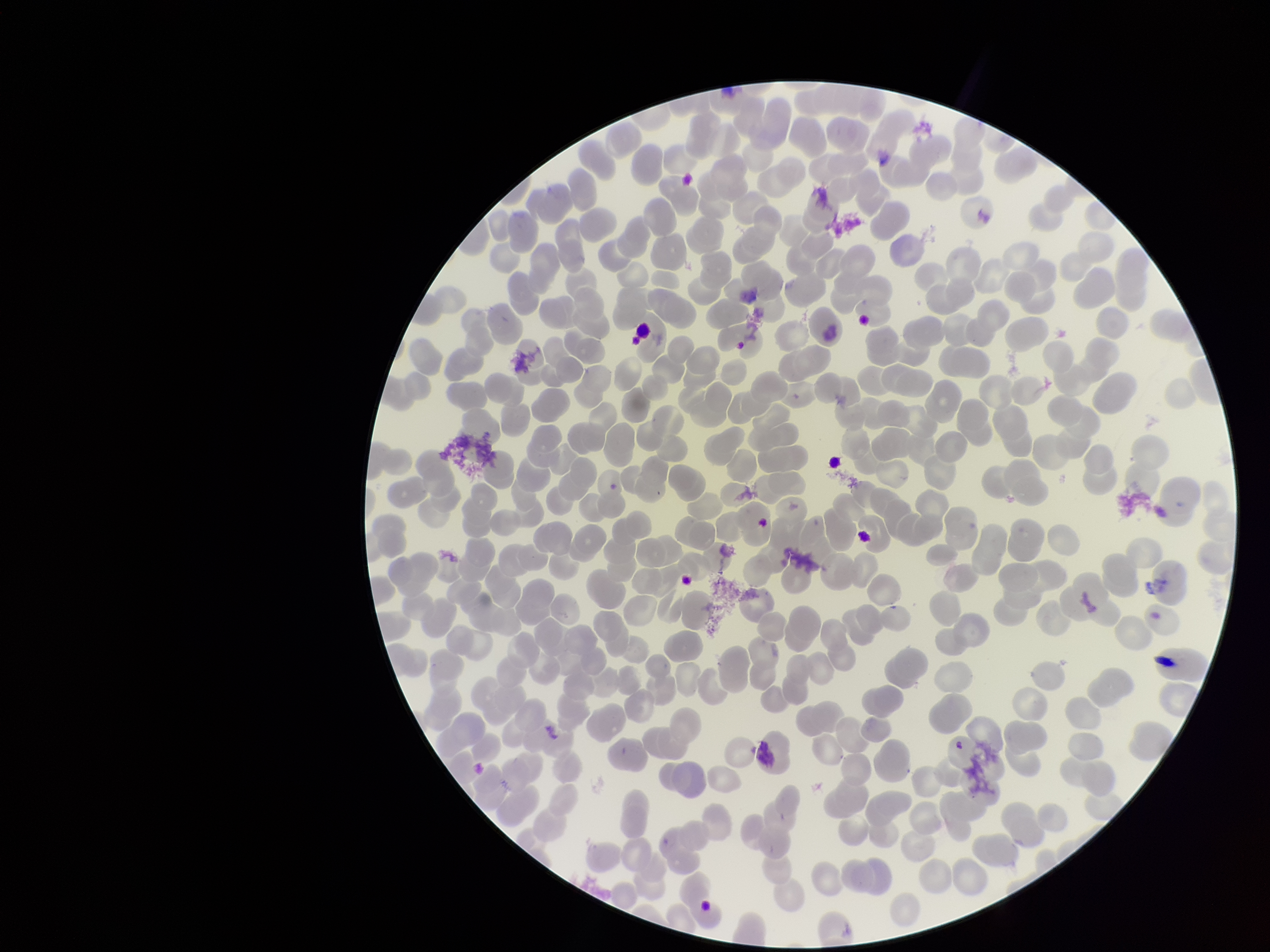 Single field of view. Giemsa stain. Image is 1270×952 pixels. Patient malaria status: positive. Photographed through the microscope eyepiece with a smartphone camera. Parasitized red blood cells: none identified. Species reported for this patient: Plasmodium falciparum. Preparation: thin. Parasitized red blood cell count: 0. Red blood cell count: 266.